Classify this cell by malaria status.
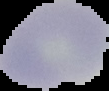

It is uninfected.

From a thin blood smear. Segmented cell region on a black background. Image is 109×91 pixels.